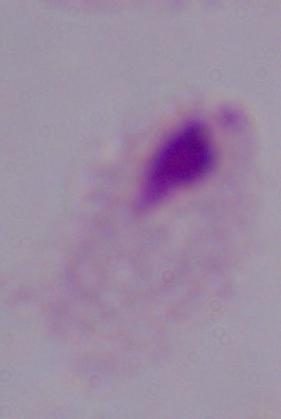
identification = trichomonad
modality = micrograph
magnification = 1000x